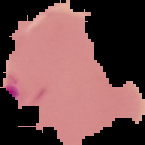
{
  "image_type": "segmented cell region with the area outside set to black",
  "image_size": "145×145 pixels",
  "preparation": "thin blood smear",
  "malaria_status": "parasitized"
}